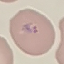

malaria status = parasitized
image type = cell patch, automatically extracted from a larger field of view and resized to 64 × 64 pixels
preparation = thin smear
stain = Giemsa
capture = smartphone camera at the microscope eyepiece